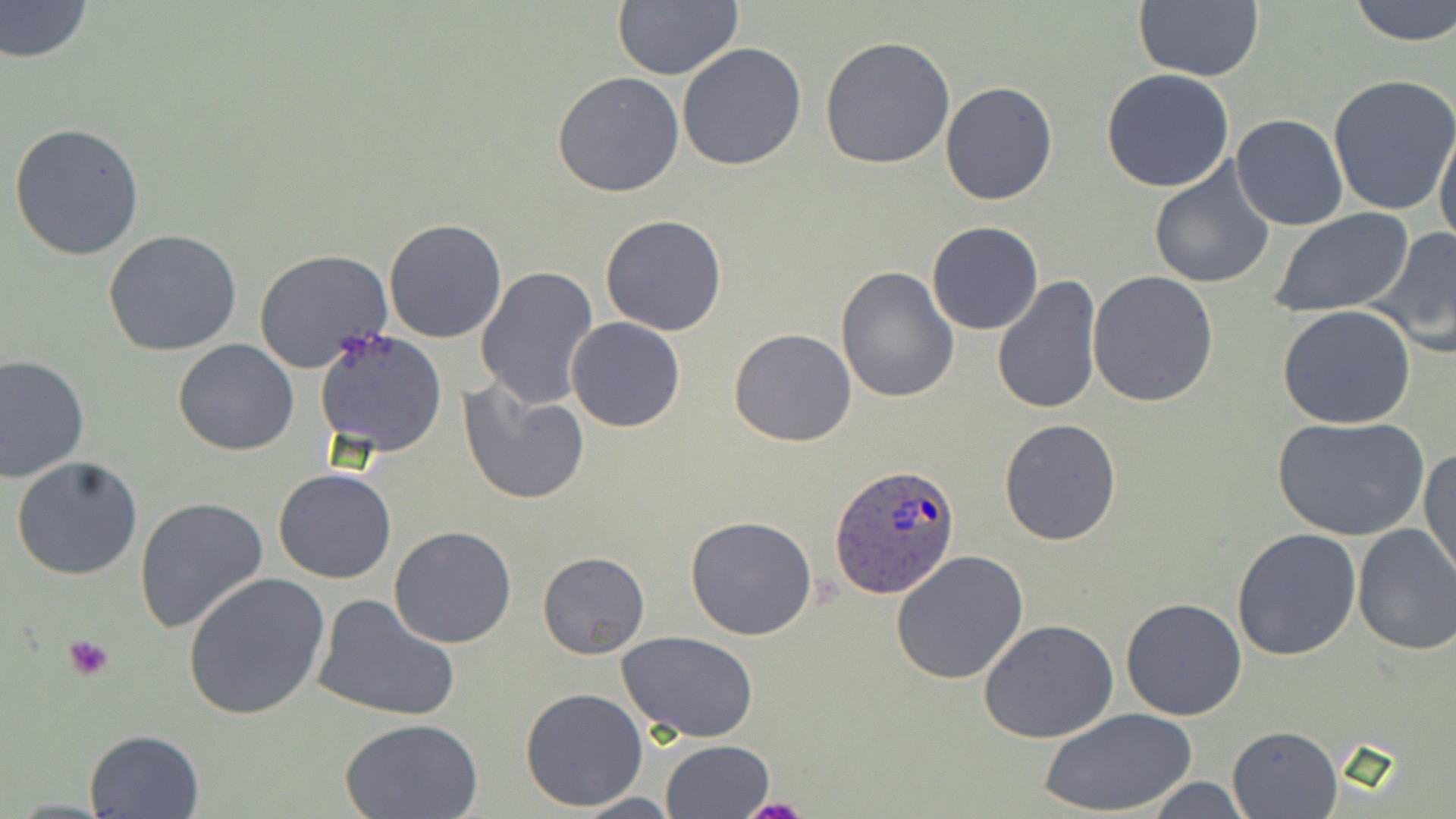
Summary:
  - Coordinate format: approximate bounding boxes as named x1/y1/x2/y2 corners in pixels
  - Platelet locations: (x1=61, y1=634, x2=115, y2=682), (x1=740, y1=795, x2=814, y2=818)
  - Plasmodium ovale-infected red blood cell locations: (x1=830, y1=465, x2=958, y2=601)
  - Uninfected red blood cell locations: (x1=0, y1=0, x2=94, y2=63), (x1=1131, y1=0, x2=1263, y2=84), (x1=1347, y1=0, x2=1456, y2=45), (x1=611, y1=2, x2=742, y2=81), (x1=822, y1=37, x2=955, y2=171), (x1=677, y1=42, x2=806, y2=171), (x1=1101, y1=70, x2=1235, y2=192), (x1=552, y1=72, x2=685, y2=197), (x1=1327, y1=72, x2=1456, y2=215), (x1=940, y1=81, x2=1058, y2=205), (x1=1231, y1=113, x2=1348, y2=231), (x1=1434, y1=118, x2=1456, y2=253), (x1=8, y1=123, x2=145, y2=260), (x1=1147, y1=156, x2=1277, y2=288), (x1=1267, y1=209, x2=1418, y2=317), (x1=600, y1=215, x2=728, y2=336), (x1=383, y1=218, x2=507, y2=343), (x1=927, y1=221, x2=1043, y2=335), (x1=1370, y1=226, x2=1456, y2=359), (x1=103, y1=229, x2=243, y2=356), (x1=254, y1=249, x2=394, y2=375), (x1=475, y1=266, x2=601, y2=410), (x1=835, y1=266, x2=960, y2=403), (x1=1087, y1=271, x2=1218, y2=408), (x1=993, y1=276, x2=1104, y2=416), (x1=1277, y1=305, x2=1419, y2=430), (x1=567, y1=318, x2=685, y2=433), (x1=729, y1=327, x2=857, y2=446), (x1=314, y1=329, x2=448, y2=458), (x1=173, y1=340, x2=299, y2=456), (x1=0, y1=355, x2=89, y2=481), (x1=460, y1=380, x2=589, y2=505), (x1=1273, y1=414, x2=1431, y2=540), (x1=1000, y1=418, x2=1122, y2=545), (x1=1419, y1=444, x2=1456, y2=584), (x1=10, y1=455, x2=143, y2=582), (x1=273, y1=467, x2=398, y2=584), (x1=136, y1=496, x2=268, y2=635), (x1=684, y1=516, x2=817, y2=640), (x1=1352, y1=523, x2=1456, y2=656), (x1=388, y1=527, x2=517, y2=648), (x1=1231, y1=528, x2=1361, y2=662), (x1=537, y1=550, x2=650, y2=658), (x1=891, y1=550, x2=1028, y2=686), (x1=182, y1=573, x2=331, y2=721), (x1=310, y1=593, x2=460, y2=724), (x1=1120, y1=597, x2=1249, y2=721), (x1=977, y1=618, x2=1119, y2=743), (x1=617, y1=631, x2=761, y2=743), (x1=519, y1=686, x2=649, y2=812), (x1=1042, y1=708, x2=1196, y2=818), (x1=339, y1=717, x2=487, y2=818), (x1=1226, y1=724, x2=1344, y2=818), (x1=82, y1=729, x2=206, y2=818), (x1=660, y1=739, x2=777, y2=818), (x1=1140, y1=775, x2=1253, y2=817), (x1=573, y1=793, x2=683, y2=818)
  - Slide-level diagnosis: Plasmodium ovale
  - Stain: May-Grünwald-Giemsa
  - Field of view: one of a larger specimen
  - Modality: optical microscopy
  - Magnification: 1000x
  - Image size: 1456×819 pixels
  - Preparation: thin blood smear